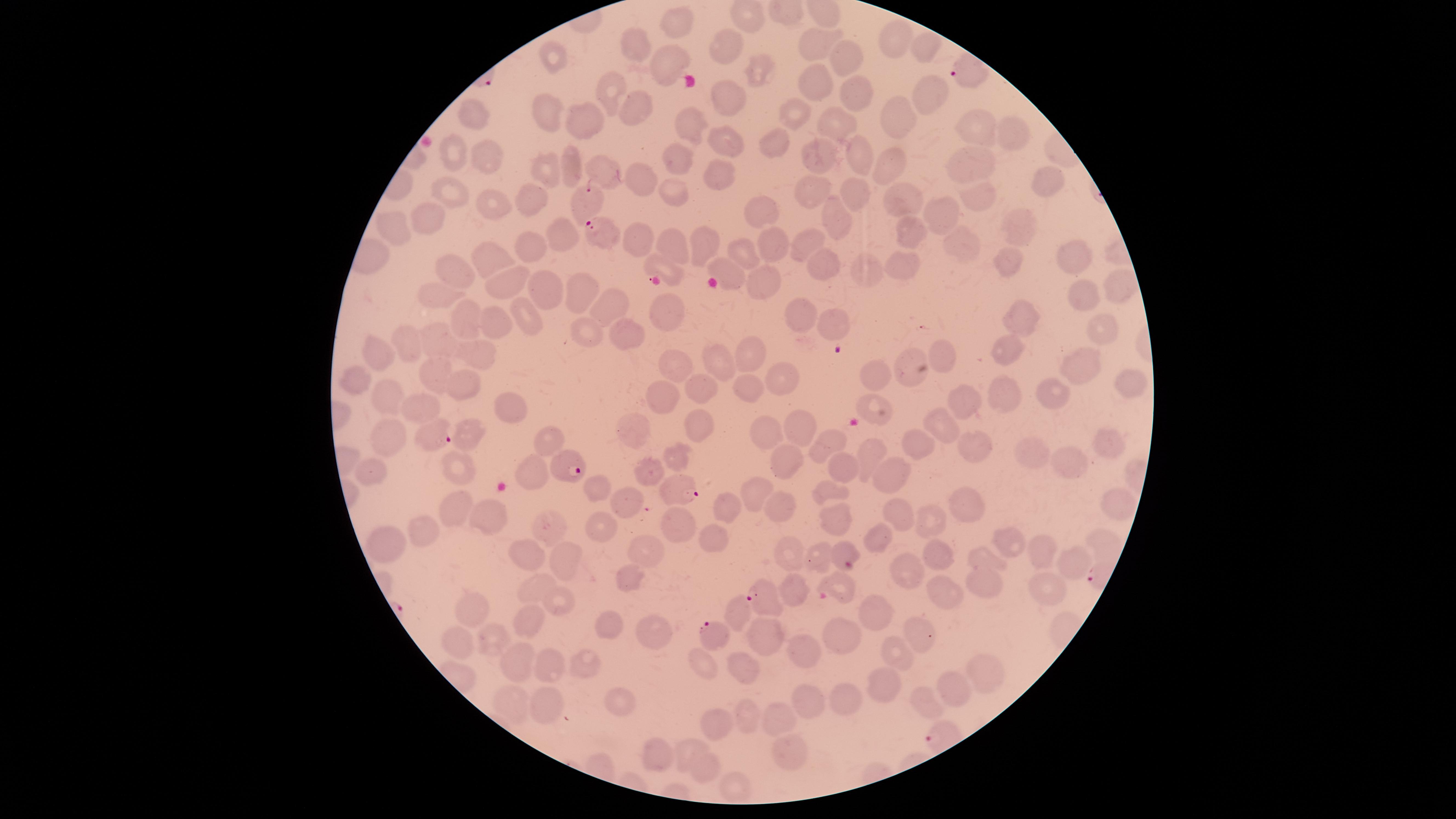

{
  "capture": "smartphone photograph through the microscope eyepiece",
  "field_of_view": "single",
  "presence": "malaria parasites seen",
  "visible_region": "circular",
  "stain": "Giemsa",
  "image_size": "1456×819 pixels",
  "parasitized_red_blood_cells": "approximate marker points as (x, y) in pixels: (967, 69), (590, 198), (602, 235), (438, 433), (565, 465), (680, 490), (765, 595), (711, 634)",
  "preparation": "thin smear of blood",
  "species": "Plasmodium falciparum",
  "uninfected_red_blood_cells": "approximate marker points as (x, y) in pixels: (677, 18), (898, 38), (637, 43), (819, 45), (723, 46), (922, 50), (558, 59), (665, 59), (850, 59), (755, 67), (819, 81), (863, 87), (929, 90), (616, 93), (729, 96), (636, 103), (549, 110), (802, 110), (468, 116), (592, 116), (898, 116), (833, 122), (693, 123), (976, 128), (1010, 129), (727, 139), (781, 145), (856, 149), (451, 152), (822, 156), (483, 158), (677, 158), (962, 160), (892, 163), (547, 164), (573, 164), (715, 169), (603, 170), (636, 176), (1044, 179), (806, 189), (453, 191), (680, 194), (532, 195), (979, 198), (851, 199), (908, 199), (495, 202), (765, 210), (940, 212), (426, 219), (836, 224), (1015, 224), (394, 231), (905, 231), (556, 236), (701, 238), (642, 242), (771, 242), (804, 243), (531, 244), (673, 246), (953, 246), (489, 255), (1081, 256), (742, 257), (1009, 263), (813, 266), (861, 266), (898, 266), (660, 268), (463, 272), (730, 278), (762, 279), (507, 284), (544, 286), (1119, 290), (439, 294), (587, 295), (1087, 298), (612, 305), (528, 313), (669, 313), (1021, 314), (469, 319), (796, 319), (498, 324), (833, 327), (590, 328), (1102, 331), (631, 334), (439, 337), (414, 342), (1003, 344), (751, 351), (946, 352), (383, 353), (481, 353), (907, 359), (722, 361), (681, 365), (1079, 365), (437, 371), (352, 374), (784, 378), (878, 378), (1134, 379), (702, 383), (465, 386), (749, 389), (1001, 390), (665, 392), (1053, 393), (390, 396), (878, 407), (972, 408), (428, 410), (517, 410), (697, 421), (638, 426), (770, 426), (807, 426), (942, 427), (545, 433), (474, 435), (380, 439), (827, 439), (916, 445), (1102, 446), (979, 450), (1035, 451), (870, 454), (674, 455), (786, 461), (1065, 461), (454, 463), (841, 465), (368, 470), (535, 470), (647, 474), (889, 474), (596, 482), (828, 488), (754, 493), (967, 499), (1113, 502), (458, 503), (628, 503), (784, 505), (487, 513), (732, 513), (901, 514), (836, 516), (929, 516), (676, 526), (558, 528), (428, 529), (606, 529), (880, 536), (713, 538), (1012, 540), (645, 543), (395, 544), (524, 552), (938, 552), (1035, 552), (845, 553), (818, 554), (984, 556), (791, 557), (559, 559), (1072, 561), (904, 570), (630, 579), (1046, 581), (840, 582), (792, 583), (992, 585), (535, 586), (951, 587), (561, 599), (477, 607), (881, 616), (529, 621), (609, 625), (766, 630), (657, 636), (843, 636), (917, 637), (493, 640), (466, 642), (797, 647), (890, 650), (511, 657), (579, 661), (543, 663), (742, 664), (709, 665), (988, 668), (952, 684), (885, 687), (620, 695), (847, 695), (515, 699), (545, 699), (807, 705), (928, 706), (750, 712), (776, 717), (725, 725), (691, 748), (788, 752), (650, 754), (707, 764), (739, 788)"
}